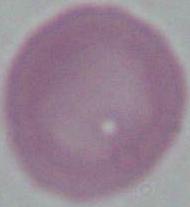

Summary:
  - Modality: micrograph
  - Magnification: 1000x
  - Identification: erythrocyte